Assess this cell for malaria.
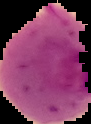

It is parasitized.

Summary:
  - Image type: segmented cell region on a black background
  - Image size: 91×124 pixels
  - Preparation: thin blood smear